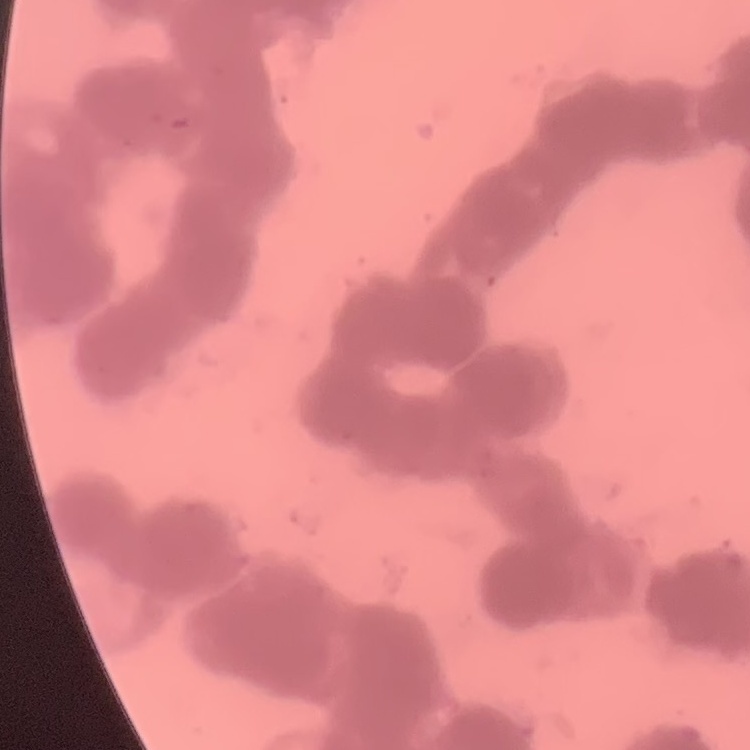

Summary:
  - Erythrocyte morphology: rouleaux formation
  - Image type: one tile cut from a larger photomicrograph
  - Stain: Field's or Giemsa
  - Preparation: thin peripheral smear